Locate every Plasmodium parasite.
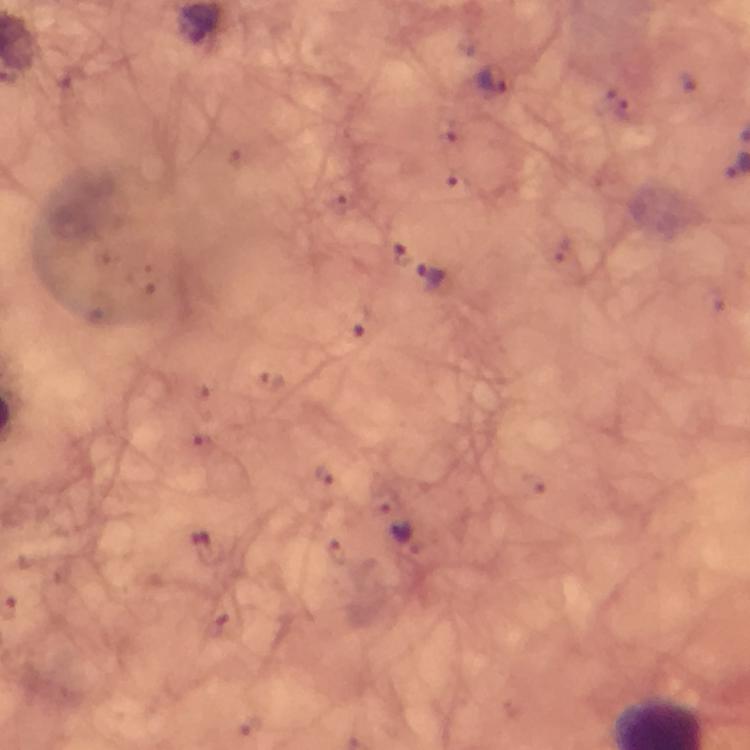

Approximate object centers, in pixels from the top-left corner.
Plasmodium parasites: (x=493, y=79), (x=433, y=278), (x=400, y=532).

preparation = thick blood film
magnification = 100x
cropped from = one field of view
capture = smartphone mounted on the microscope
image size = 750×750 pixels
stain = Giemsa
context = from a diagnostic examination for malaria
immersion oil = used